Comment on the morphology of the red blood cells.
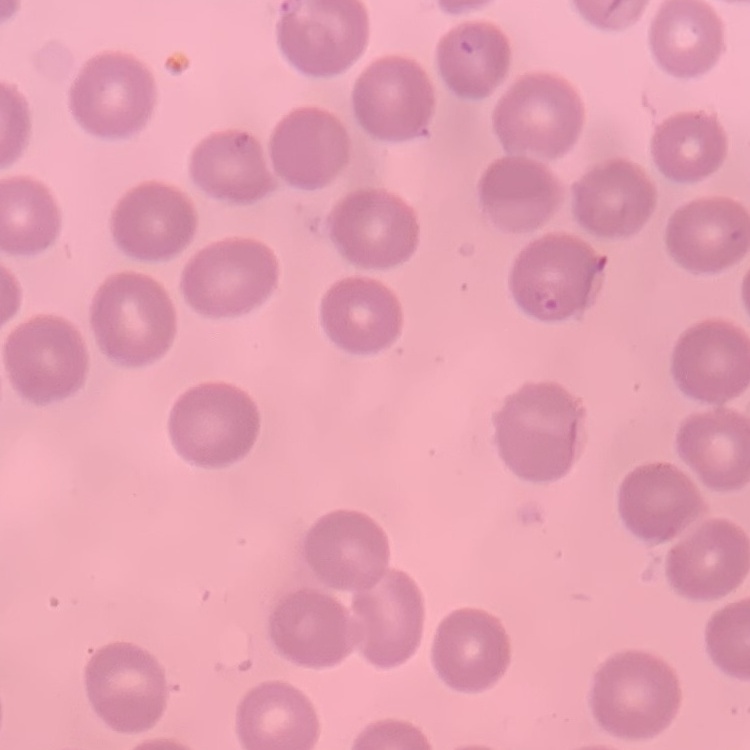

They show no rouleaux formation.

{
  "preparation": "thin blood smear",
  "image_type": "one tile cut from a larger photomicrograph",
  "stain": "Field's or Giemsa"
}